Describe the morphology of the erythrocytes.
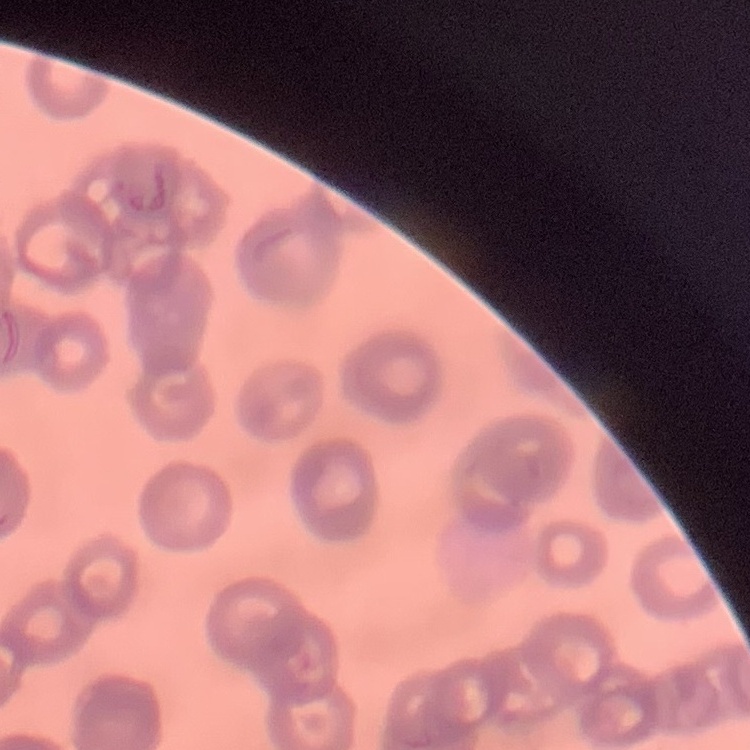

They show rouleaux formation.

{
  "preparation": "thin blood smear",
  "stain": "Field's or Giemsa",
  "image_type": "square crop of a larger photomicrograph"
}